State which parasite is depicted.
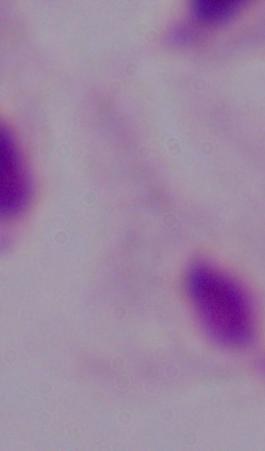

This is a trichomonad.

magnification = 1000x
modality = photomicrograph